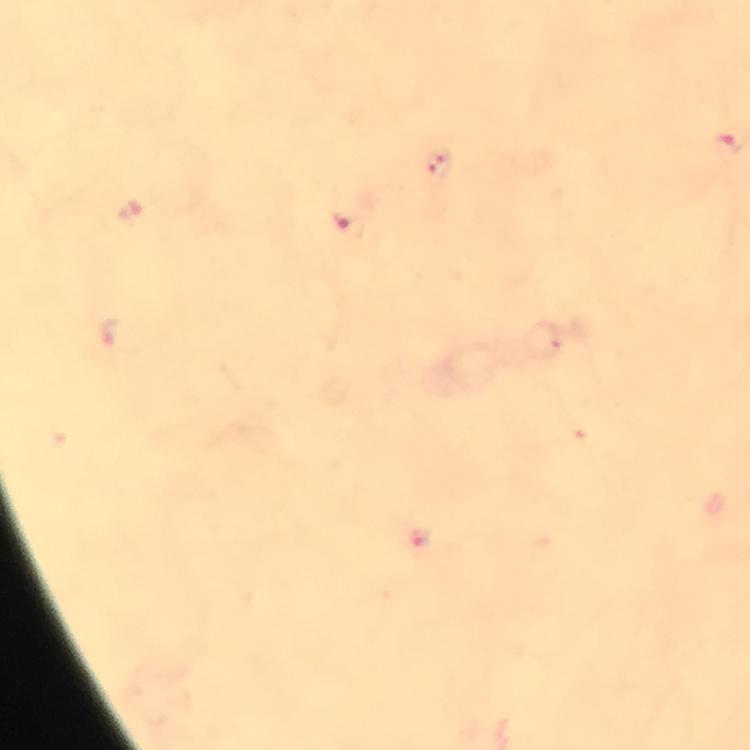

{
  "immersion_oil": "applied",
  "stain": "Giemsa",
  "capture": "smartphone photograph through a microscope",
  "image_size": "750×750 pixels",
  "plasmodium_parasite_locations": "approximate centers as (x, y) in pixels: (438, 164), (347, 224), (419, 539)",
  "cropped_from": "one field of view",
  "magnification": "100x",
  "context": "from a diagnostic examination for malaria",
  "preparation": "thick blood film"
}